Classify this cell by malaria status.
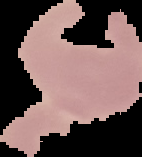

It is uninfected.

preparation = thin blood smear
image type = cell region segmented out of the field of view; surrounding area masked to black
image size = 142×157 pixels